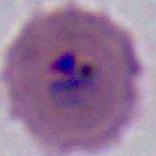
{
  "modality": "photomicrograph",
  "identification": "Plasmodium",
  "magnification": "400x or 1000x"
}